Assess this cell for malaria.
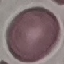
Uninfected.

Summary:
  - Image type: automatically extracted cell patch, resized to 64 × 64 pixels
  - Preparation: thin blood film
  - Stain: Giemsa
  - Capture: smartphone through the microscope eyepiece